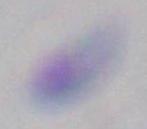
1000x magnification. Micrograph. Toxoplasma gondii is shown.